Locate the cells, classifying each as a parasitized red blood cell, an uninfected red blood cell, or a white blood cell.
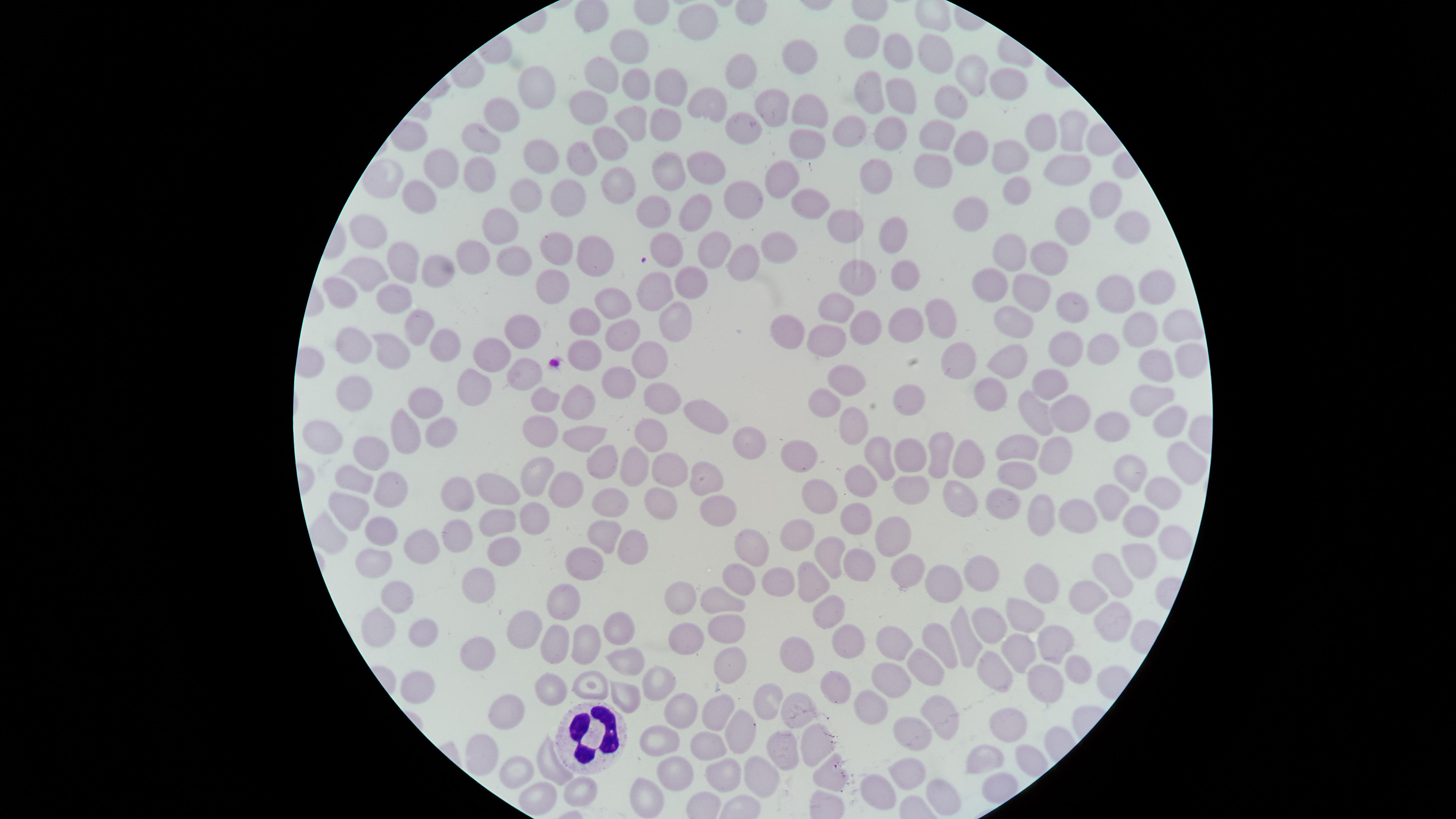
No parasitized red blood cells identified.
Approximate marker points as (x, y) in pixels.
Uninfected red blood cells: (694, 19), (633, 45), (865, 45), (898, 51), (935, 53), (801, 60), (602, 68), (744, 72), (972, 76), (633, 79), (1013, 83), (540, 85), (664, 87), (867, 87), (901, 96), (706, 100), (767, 102), (803, 106), (950, 106), (592, 109), (508, 110), (631, 124), (667, 126), (747, 130), (886, 131), (1069, 131), (1042, 133), (860, 135), (938, 136), (483, 137), (803, 140), (608, 144), (969, 146), (1007, 146), (538, 155), (584, 159), (438, 165), (1072, 167), (667, 168), (783, 168), (876, 168), (707, 169), (934, 170), (479, 173), (385, 177), (1022, 185), (619, 186), (566, 192), (527, 194), (803, 197), (420, 198), (748, 198), (1104, 203), (695, 207), (655, 210), (973, 215), (853, 223), (498, 226), (1074, 227), (1124, 229), (897, 232), (780, 240), (369, 242), (556, 245), (661, 250), (719, 251), (471, 256), (590, 256), (1009, 257), (1041, 258), (400, 260), (514, 260), (748, 263), (435, 264), (860, 269), (368, 276), (902, 277), (552, 280), (697, 281), (990, 286), (1160, 286), (343, 288), (654, 291), (1032, 291), (1120, 298), (388, 299), (616, 304), (1078, 306), (841, 312), (673, 316), (906, 318), (589, 321), (943, 322), (1180, 323), (1011, 326), (415, 329), (795, 329), (859, 330), (527, 331), (1140, 331), (629, 335), (439, 339), (827, 339), (1072, 346), (359, 348), (1098, 348), (395, 352), (593, 352), (1014, 352), (494, 356), (652, 356), (1183, 357), (1156, 365), (952, 372), (523, 373), (842, 375), (1045, 379), (624, 381), (467, 392), (354, 393), (663, 393), (546, 395), (988, 395), (905, 396), (1149, 397), (577, 402), (424, 403), (824, 410), (702, 415), (1037, 415), (1069, 415), (1165, 419), (406, 425), (441, 426), (539, 426), (861, 427), (1113, 427), (585, 431), (657, 431), (324, 432), (744, 443), (1055, 449), (943, 450), (1019, 450), (365, 453), (911, 456), (881, 457), (971, 457), (605, 461), (798, 461), (1184, 463), (632, 466), (671, 468), (1135, 469), (1011, 474), (543, 479), (860, 480), (345, 481), (911, 481), (697, 484), (1160, 490), (499, 491), (565, 493), (954, 493), (388, 494), (812, 496), (463, 498), (1110, 500), (1005, 501), (609, 502), (662, 503), (342, 505), (719, 510), (534, 517), (852, 518), (1085, 519), (1037, 520), (1139, 520), (494, 523), (324, 529), (891, 529), (378, 533), (461, 536), (600, 540), (790, 543), (1161, 544), (750, 545), (421, 546), (502, 548), (629, 548), (830, 554), (1132, 562), (373, 565), (855, 565), (583, 568), (897, 568), (1109, 571), (983, 575), (1046, 577), (744, 581), (941, 582), (478, 583), (775, 584), (816, 585), (1079, 590), (396, 593), (565, 593), (720, 599), (682, 601), (832, 614), (1025, 614), (381, 621), (1107, 621), (982, 626), (619, 629), (425, 630), (522, 630), (720, 632), (548, 633), (686, 638), (936, 638), (847, 642), (890, 642), (957, 642), (1059, 645), (588, 646), (475, 653), (1018, 655), (792, 656), (624, 661), (1078, 666), (727, 667), (995, 669), (924, 671), (891, 678), (838, 683), (650, 684), (1036, 684), (422, 686), (552, 689), (591, 689), (867, 699), (620, 701), (797, 701), (760, 703), (682, 706), (515, 708), (721, 710), (938, 713), (1011, 723), (743, 730), (664, 733), (911, 738), (811, 744), (708, 746), (986, 754), (487, 755), (780, 755), (511, 768), (549, 770), (909, 770), (671, 773), (721, 773), (759, 774), (828, 774), (571, 792), (876, 792), (935, 792), (643, 794), (532, 797).
White blood cells: (591, 739).

Image is 1456×819 pixels. One field of view of the specimen. Circular visible region. Thin blood film. Giemsa stain. Smartphone photograph through the microscope eyepiece.